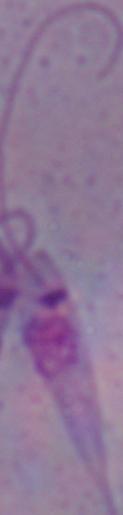
Summary:
  - Magnification: 1000x
  - Identification: Leishmania
  - Modality: micrograph